Assess the morphology of the erythrocytes.
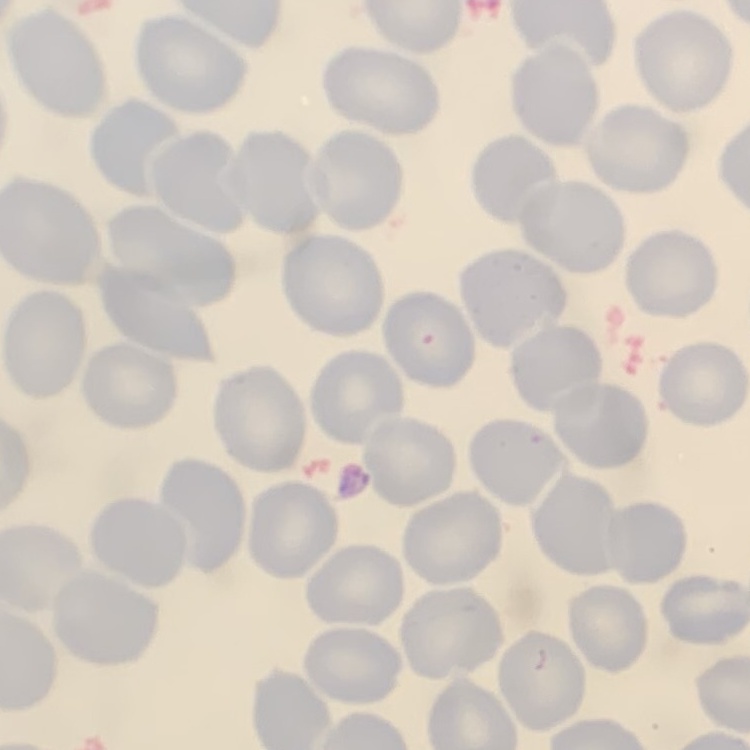

They show no rouleaux formation.

Field's or Giemsa stain. Thin peripheral smear. Square crop of a larger photomicrograph.